Classify this cell by malaria status.
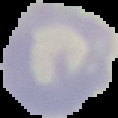

Uninfected.

Summary:
  - Image type: segmented cell region on a black background
  - Preparation: thin blood smear
  - Image size: 118×118 pixels